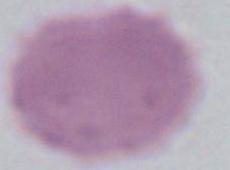
magnification = 1000x
modality = micrograph
identification = erythrocyte